Name the blood parasite species.
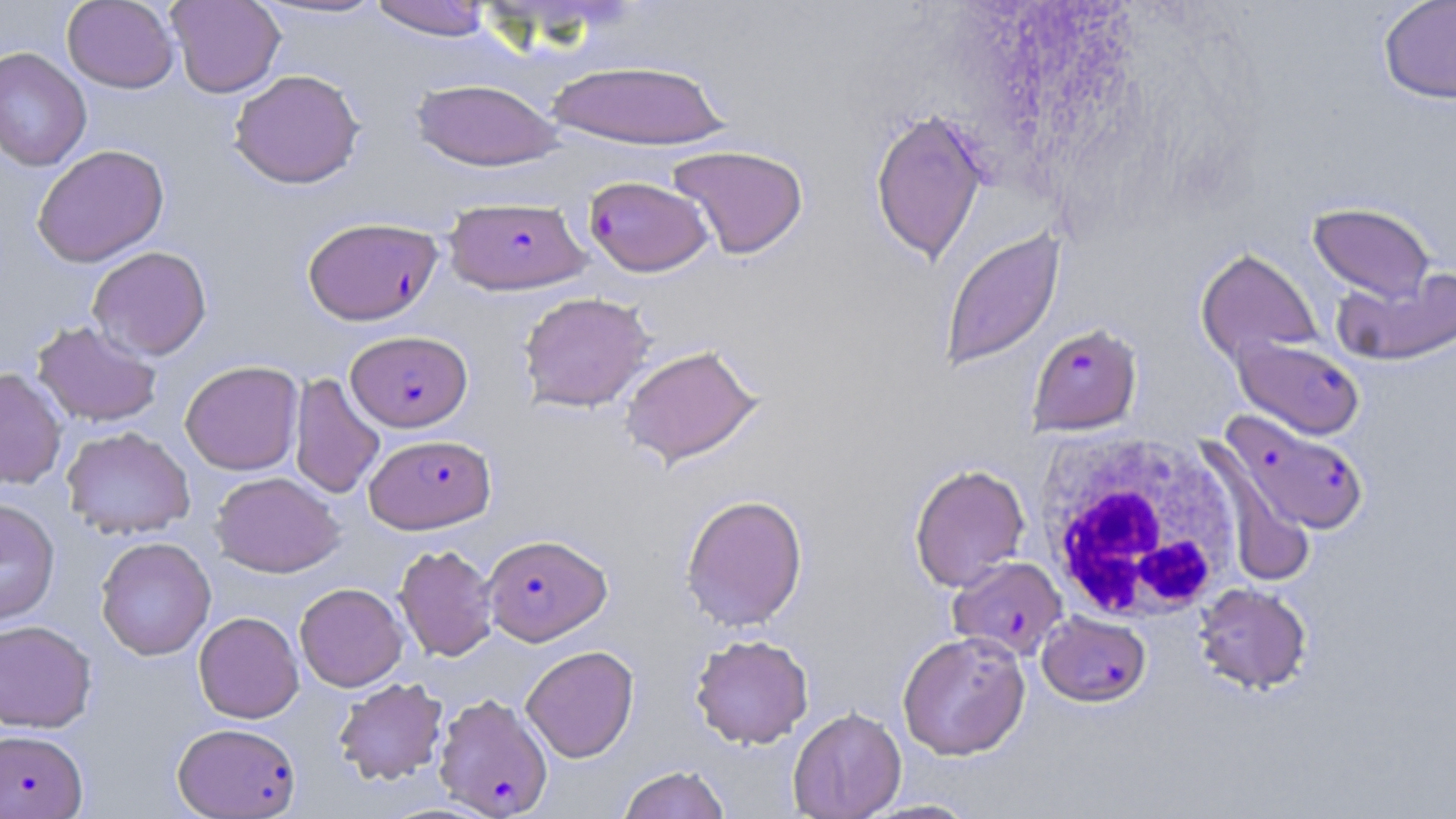
Plasmodium falciparum.

Approximate bounding boxes as [x1, y1, x2, y2] in pixels. Uninfected red blood cell locations: [62, 0, 179, 93], [166, 0, 285, 98], [250, 0, 391, 21], [367, 0, 498, 40], [1378, 0, 1456, 104], [0, 47, 92, 171], [546, 59, 730, 149], [228, 69, 365, 189], [410, 78, 563, 171], [869, 107, 989, 265], [31, 144, 169, 267], [668, 144, 809, 259], [1308, 202, 1436, 302], [939, 227, 1065, 372], [88, 246, 212, 360], [1195, 247, 1323, 365], [1333, 266, 1456, 368], [518, 291, 655, 413], [32, 319, 163, 428], [619, 343, 763, 467], [180, 360, 303, 475], [0, 368, 67, 489], [287, 373, 382, 500], [61, 426, 195, 540], [1196, 441, 1317, 589], [909, 462, 1031, 592], [210, 471, 344, 577], [680, 493, 808, 631], [0, 498, 60, 625], [95, 536, 216, 661], [393, 544, 499, 661], [294, 582, 408, 691], [1193, 582, 1313, 694], [193, 611, 304, 723], [0, 619, 96, 733], [897, 630, 1031, 760], [690, 633, 814, 748], [521, 645, 639, 763], [333, 677, 449, 785], [788, 706, 906, 819], [618, 765, 731, 819], [860, 798, 982, 818]. Plasmodium falciparum-infected red blood cell locations: [584, 176, 713, 277], [445, 196, 591, 295], [302, 216, 443, 325], [1027, 323, 1143, 436], [346, 330, 472, 432], [1231, 335, 1365, 440], [1223, 410, 1370, 536], [364, 433, 497, 534], [482, 533, 611, 645], [948, 556, 1068, 661], [1036, 610, 1151, 706], [434, 692, 553, 818], [172, 722, 302, 818], [0, 730, 88, 817]. White blood cell locations: [1033, 429, 1246, 625]. May-Grünwald-Giemsa-stained preparation. Captured at 1000x magnification. Thin blood smear. Optical microscopy. One field of a larger specimen. Image is 1456×819 pixels.